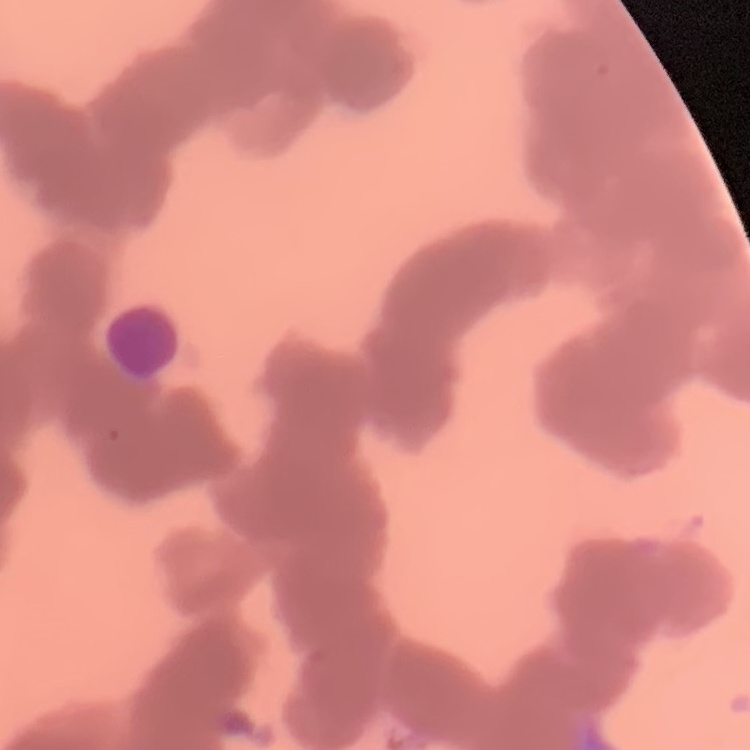
erythrocyte morphology = rouleaux formation
image type = one tile cut from a larger photomicrograph
preparation = thin blood smear
stain = Field's or Giemsa